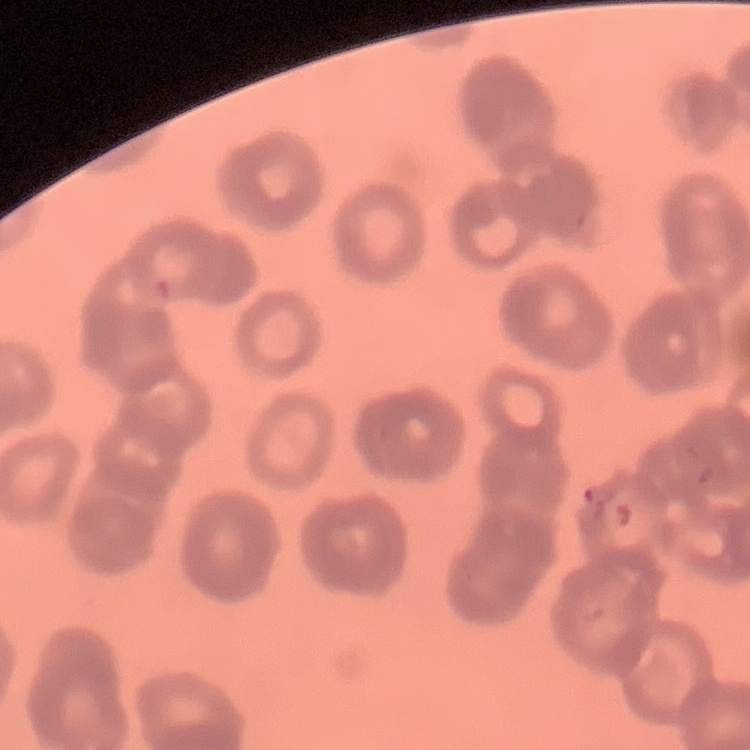

{
  "erythrocyte_morphology": "rouleaux formation",
  "stain": "Field's or Giemsa",
  "preparation": "thin blood film",
  "image_type": "one tile cut from a larger photomicrograph"
}